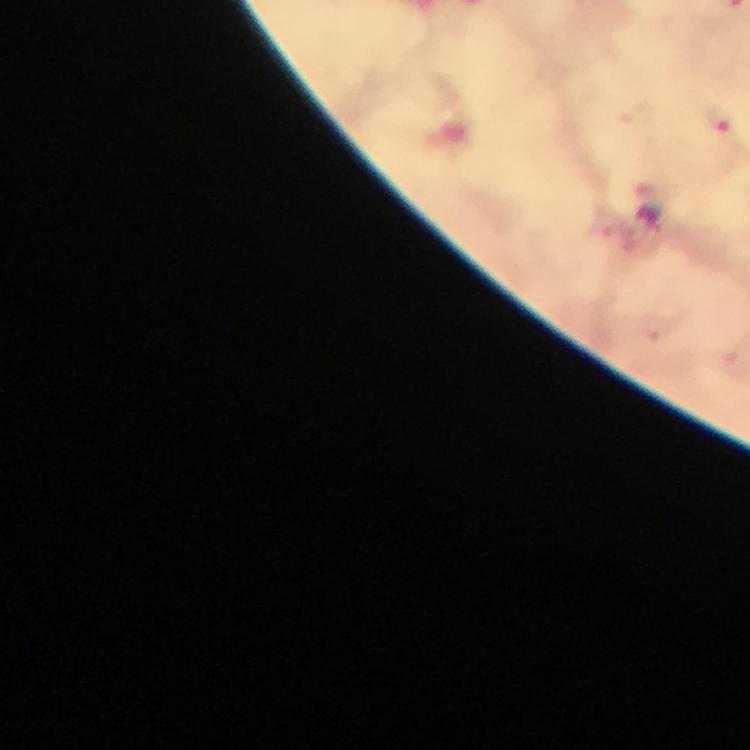
magnification: 100x
capture: smartphone mounted on the microscope
image_size: 750×750 pixels
stain: Giemsa
malaria_parasite_locations: 'approximate centers as {x, y} in pixels: {640, 116}, {719, 124}'
preparation: thick blood film
immersion_oil: used
cropped_from: one field of view
context: from a diagnostic examination for malaria